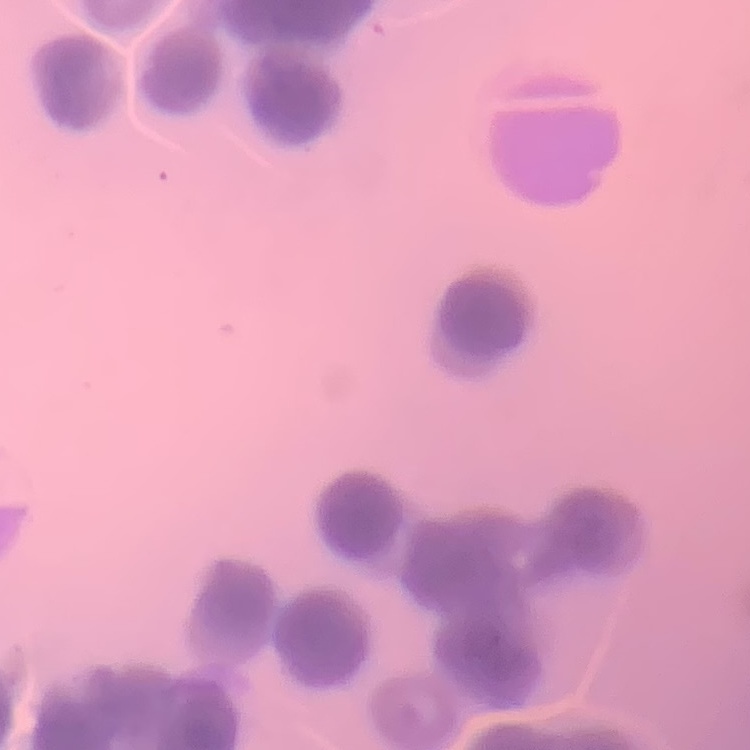
The erythrocytes show rouleaux formation. Stained with either Field's or Giemsa. One tile cut from a larger photomicrograph. Thin blood smear.